Give the extent of all Trypanosoma brucei.
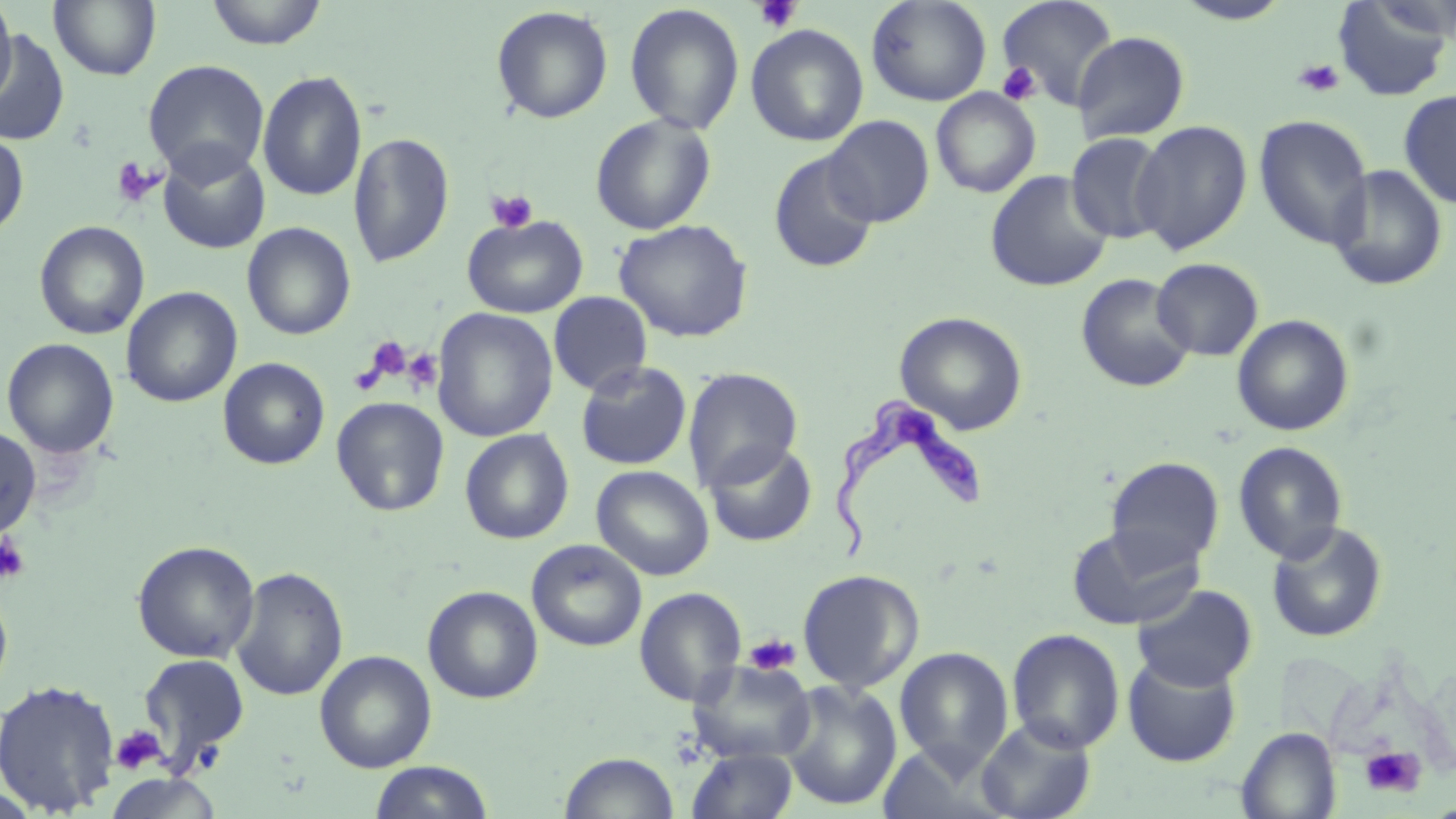

Approximate bounding boxes as (x1,y1)-(x2,y2) corner pairs in pixels.
Trypanosoma brucei: (825,392)-(993,565).

slide_level_diagnosis: Trypanosoma brucei
magnification: 1000x
stain: May-Grünwald-Giemsa
platelet_locations: 'approximate bounding boxes as (x1,y1)-(x2,y2) corner pairs in pixels: (753,0)-(801,33), (1294,58)-(1344,97), (997,61)-(1042,107), (110,156)-(165,209), (486,189)-(538,234), (362,336)-(412,385), (403,348)-(443,394), (0,532)-(30,585), (743,631)-(800,677), (111,725)-(166,774), (1358,744)-(1425,798)'
field_of_view: one of a larger specimen
image_size: 1456×819 pixels
preparation: thin blood smear
uninfected_red_blood_cell_locations: 'approximate bounding boxes as (x1,y1)-(x2,y2) corner pairs in pixels: (0,0)-(17,106), (49,0)-(162,81), (205,0)-(328,49), (866,0)-(992,106), (997,0)-(1119,110), (1332,0)-(1454,102), (1173,1)-(1292,25), (625,4)-(744,135), (491,6)-(613,124), (745,24)-(869,147), (0,30)-(70,146), (1073,31)-(1189,143), (142,60)-(270,182), (258,70)-(367,202), (930,88)-(1041,198), (1398,89)-(1456,209), (590,113)-(716,235), (823,115)-(934,227), (1253,115)-(1374,250), (1132,120)-(1253,255), (0,130)-(29,238), (1066,131)-(1171,243), (349,132)-(454,269), (157,144)-(270,254), (768,149)-(879,274), (1329,164)-(1448,291), (985,169)-(1113,292), (462,214)-(587,318), (614,219)-(753,343), (34,221)-(150,340), (242,223)-(356,340), (1151,257)-(1264,361), (1075,272)-(1195,393), (121,286)-(242,408), (548,292)-(652,396), (431,307)-(558,442), (894,312)-(1027,434), (1232,314)-(1354,436), (2,337)-(119,459), (217,357)-(331,470), (575,360)-(693,471), (682,367)-(803,490), (331,397)-(450,516), (0,425)-(42,540), (459,429)-(574,544), (704,441)-(816,547), (1232,441)-(1348,564), (1106,456)-(1224,570), (591,465)-(714,581), (1266,520)-(1388,644), (1066,523)-(1206,630), (526,539)-(647,652), (132,540)-(260,664), (230,566)-(348,701), (797,569)-(924,693), (0,583)-(14,702), (1132,583)-(1257,691), (422,585)-(543,704), (634,587)-(747,707), (1007,628)-(1125,753), (894,646)-(1014,772), (315,650)-(437,773), (137,653)-(251,770), (1122,653)-(1242,767), (689,659)-(817,763), (0,678)-(121,816), (778,679)-(902,812), (975,718)-(1097,819), (1237,727)-(1342,819), (878,743)-(1003,817), (687,748)-(799,819), (559,751)-(679,818), (368,761)-(494,818)'
modality: optical microscopy